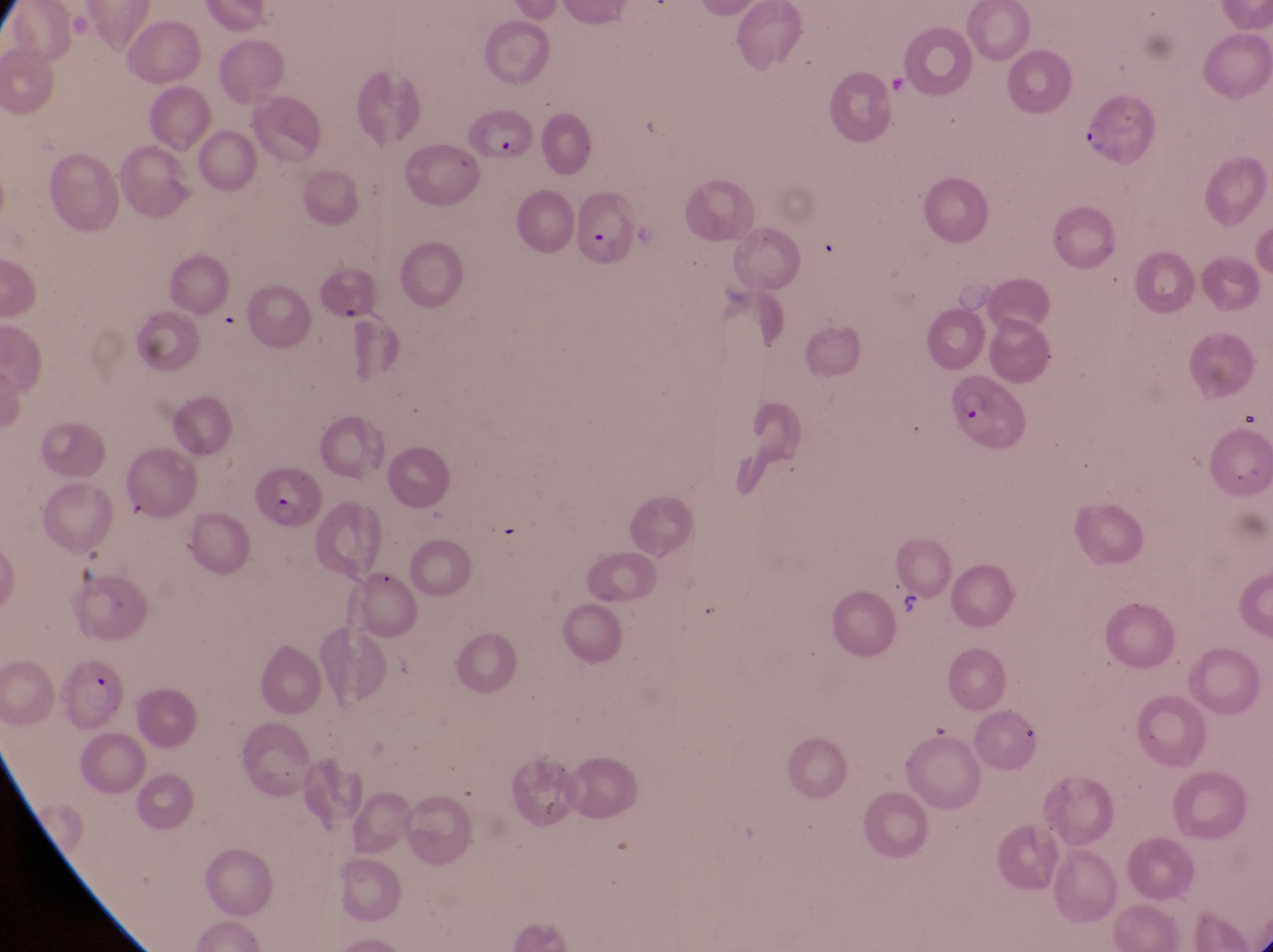
Approximate bounding boxes as left top right bottom in pixels. Parasitised red blood cell locations: 1083 92 1160 167; 464 104 531 169; 567 182 649 270; 951 367 1031 457; 244 459 322 533; 60 656 127 733. Artifact (platelet-like body, stain precipitate, or debris) locations: 893 586 928 621. Single field of view. Captured by a smartphone held over the eyepiece of an Olympus CX-23 microscope. Sample from Uganda. At a magnification of 1000x. Image is 1273×952 pixels. Thin blood smear.